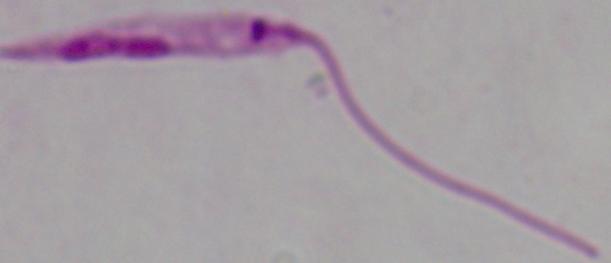

Photomicrograph. A Leishmania parasite is seen. 1000x magnification.